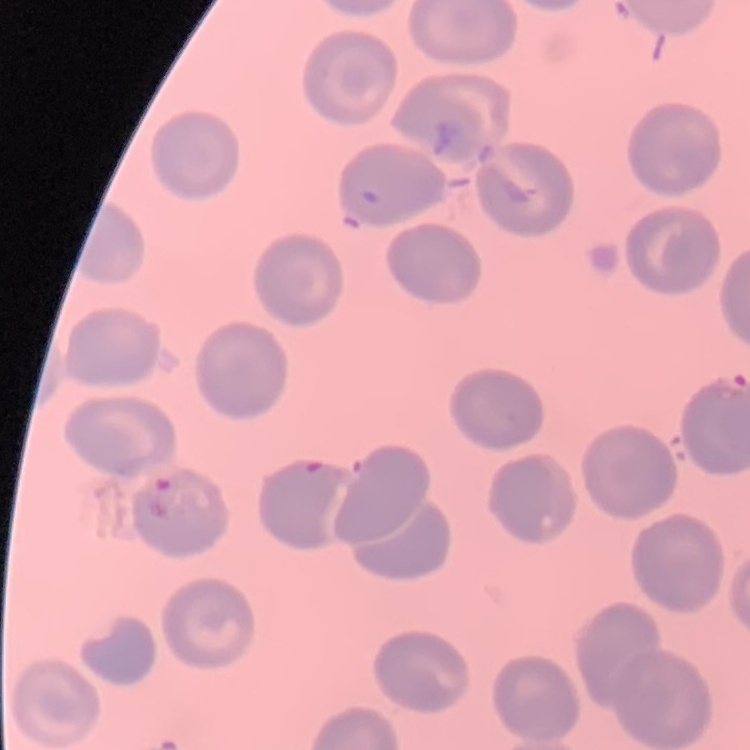

Summary:
  - Erythrocyte morphology: no rouleaux formation
  - Image type: square crop of a larger photomicrograph
  - Stain: Field's or Giemsa
  - Preparation: thin blood film